Describe the morphology of the red blood cells.
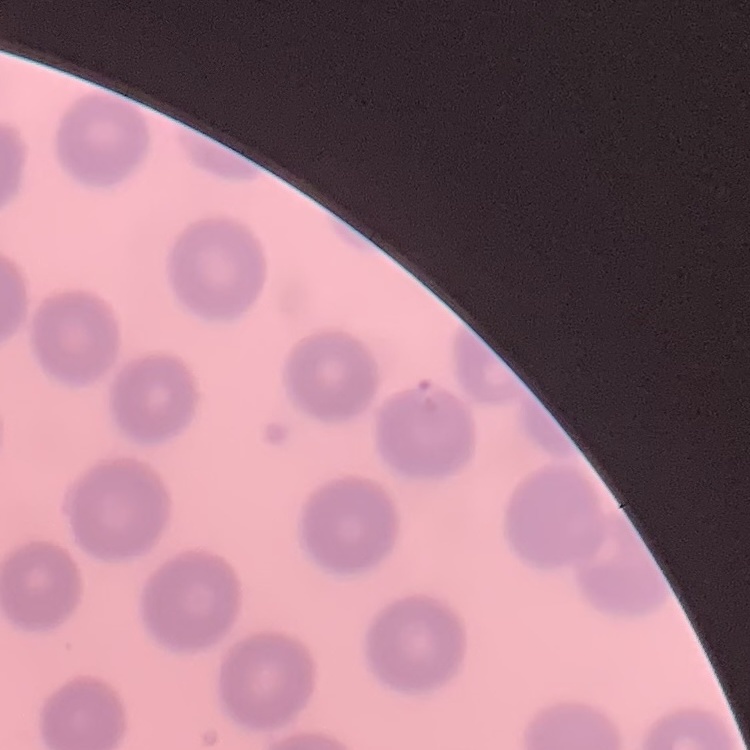
No rouleaux formation.

Summary:
  - Image type: square crop of a larger photomicrograph
  - Preparation: thin peripheral smear
  - Stain: Field's or Giemsa